Classify this cell by malaria status.
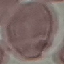
Uninfected.

{
  "stain": "Giemsa",
  "capture": "smartphone through the microscope eyepiece",
  "image_type": "cell patch, automatically extracted from a larger field of view and resized to 64 × 64 pixels",
  "preparation": "thin smear"
}